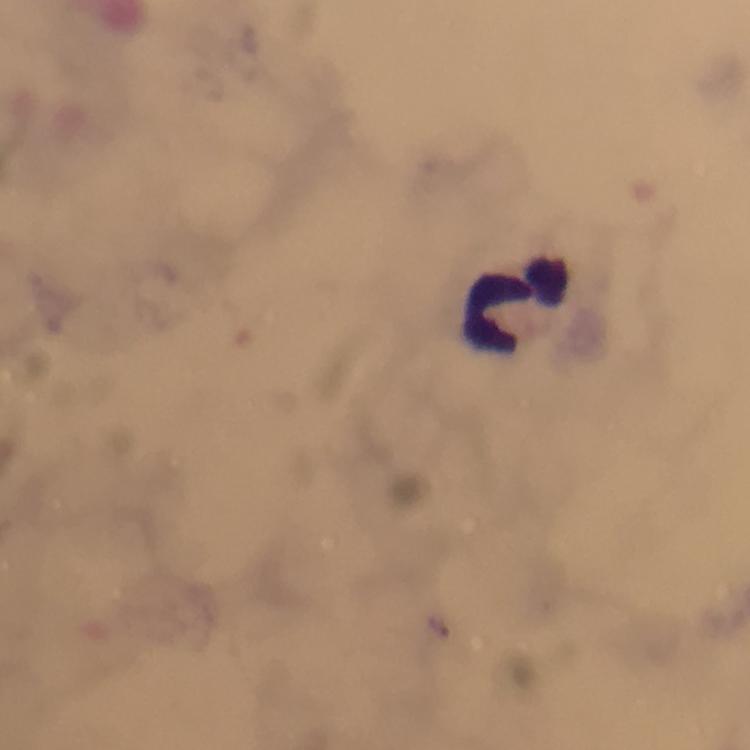
context = from a diagnostic examination for malaria
stain = Giemsa
magnification = 100x
image size = 750×750 pixels
cropped from = one field of view
leukocyte locations = approximate centers as {x, y} in pixels: {521, 304}
immersion oil = applied
capture = smartphone mounted on the microscope
Plasmodium parasites = none detected
preparation = thick smear